Identify the preparation type.
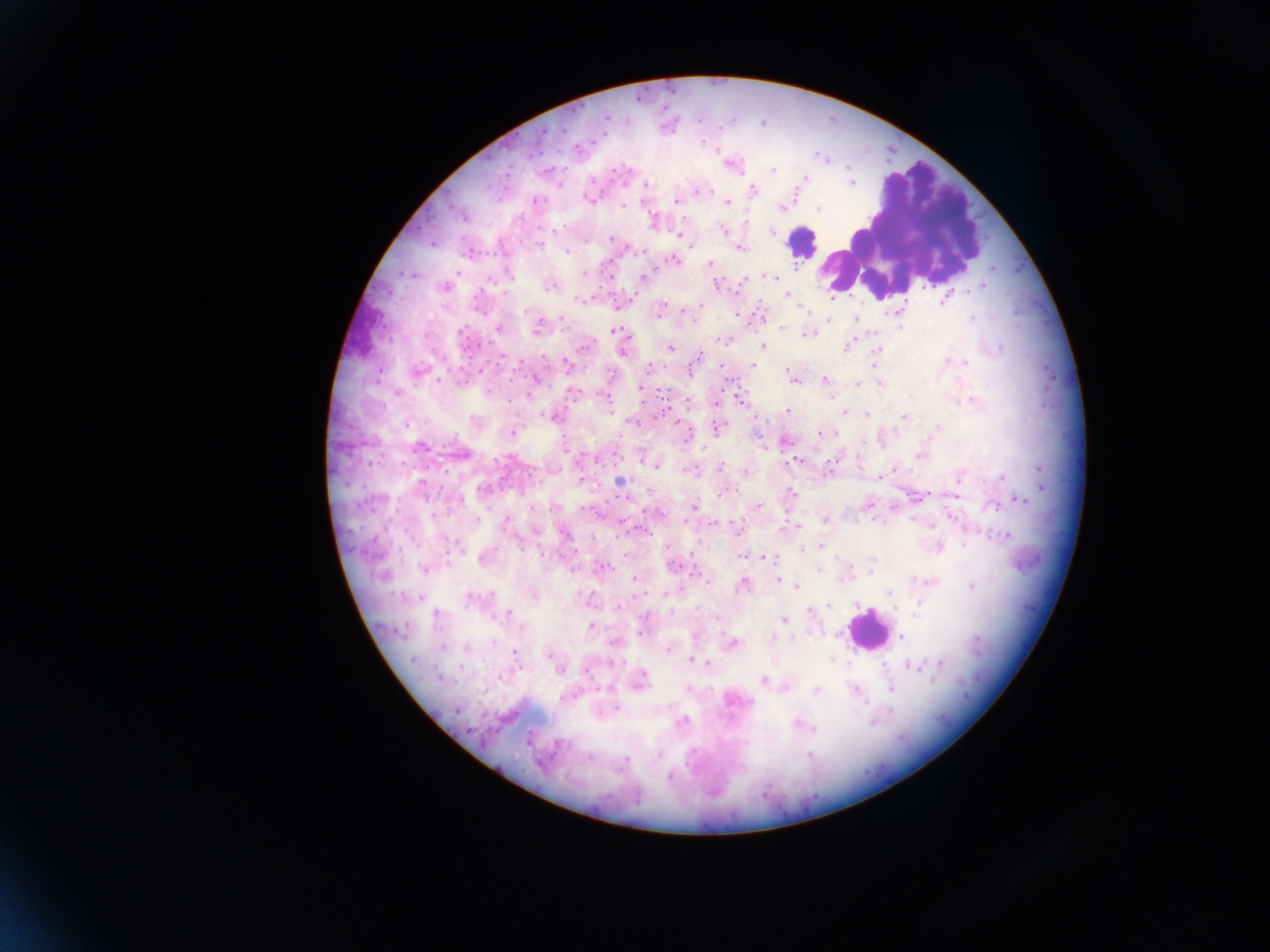

This is a thick smear.

{
  "capture": "mobile-phone photograph through a microscope",
  "image_size": "1270×952 pixels",
  "country": "Ghana",
  "malaria_parasite_locations": "approximate centers as x y in pixels: 729 163; 771 170; 804 178; 852 184; 558 185; 645 186; 752 190; 699 191; 588 198; 676 200; 725 202; 622 205; 781 207; 818 208; 463 215; 653 221; 724 231; 772 232; 679 235; 610 238; 432 242; 691 244; 540 245; 738 248; 467 252; 673 259; 711 263; 583 274; 774 276; 643 278; 744 279; 716 284; 550 285; 444 288; 787 295; 582 300; 944 300; 617 306; 697 306; 899 310; 659 312; 735 314; 762 316; 693 320; 855 320; 829 321; 538 325; 498 328; 781 328; 899 328; 616 331; 806 333; 723 340; 763 346; 846 347; 669 348; 623 351; 876 351; 752 364; 566 365; 648 367; 377 370; 417 372; 794 379; 823 381; 857 385; 880 385; 640 388; 572 392; 607 397; 740 399; 972 401; 688 402; 717 403; 788 411; 844 411; 867 415; 553 416; 903 417; 677 424; 718 428; 821 432; 512 433; 420 445; 764 448; 459 453; 641 455; 920 456; 597 459; 857 459; 794 460; 657 464; 720 467; 691 470; 892 470; 746 472; 828 472; 959 476; 1002 476; 878 477; 581 480; 618 481; 793 495; 954 495; 627 498; 1019 500; 867 504; 695 505; 757 507; 994 507; 873 519; 914 519; 506 520; 824 520; 686 521; 714 522; 735 527; 797 529; 1005 534; 822 546; 939 547; 460 549; 800 549; 742 556; 764 557; 484 558; 672 565; 603 566; 424 568; 696 573; 384 575; 635 578; 777 580; 709 581; 930 581; 743 585; 797 586; 972 586; 889 592; 532 594; 665 594; 471 599; 829 605; 616 606; 809 613; 509 614; 784 620; 591 627; 641 630; 900 637; 772 638; 731 644; 465 646; 669 649; 515 653; 693 661; 940 663; 708 664; 909 664; 558 668; 440 678; 763 680; 639 681; 785 688; 855 689; 891 689; 817 690; 733 699; 456 709; 798 724; 588 757",
  "field_of_view": "single",
  "leukocyte_locations": "approximate centers as x y in pixels: 901 230; 801 242; 361 327; 868 630"
}